Assess this cell for malaria.
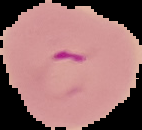

It is parasitized.

{
  "image_type": "segmented cell region on a black background",
  "preparation": "thin blood smear",
  "image_size": "142×130 pixels"
}